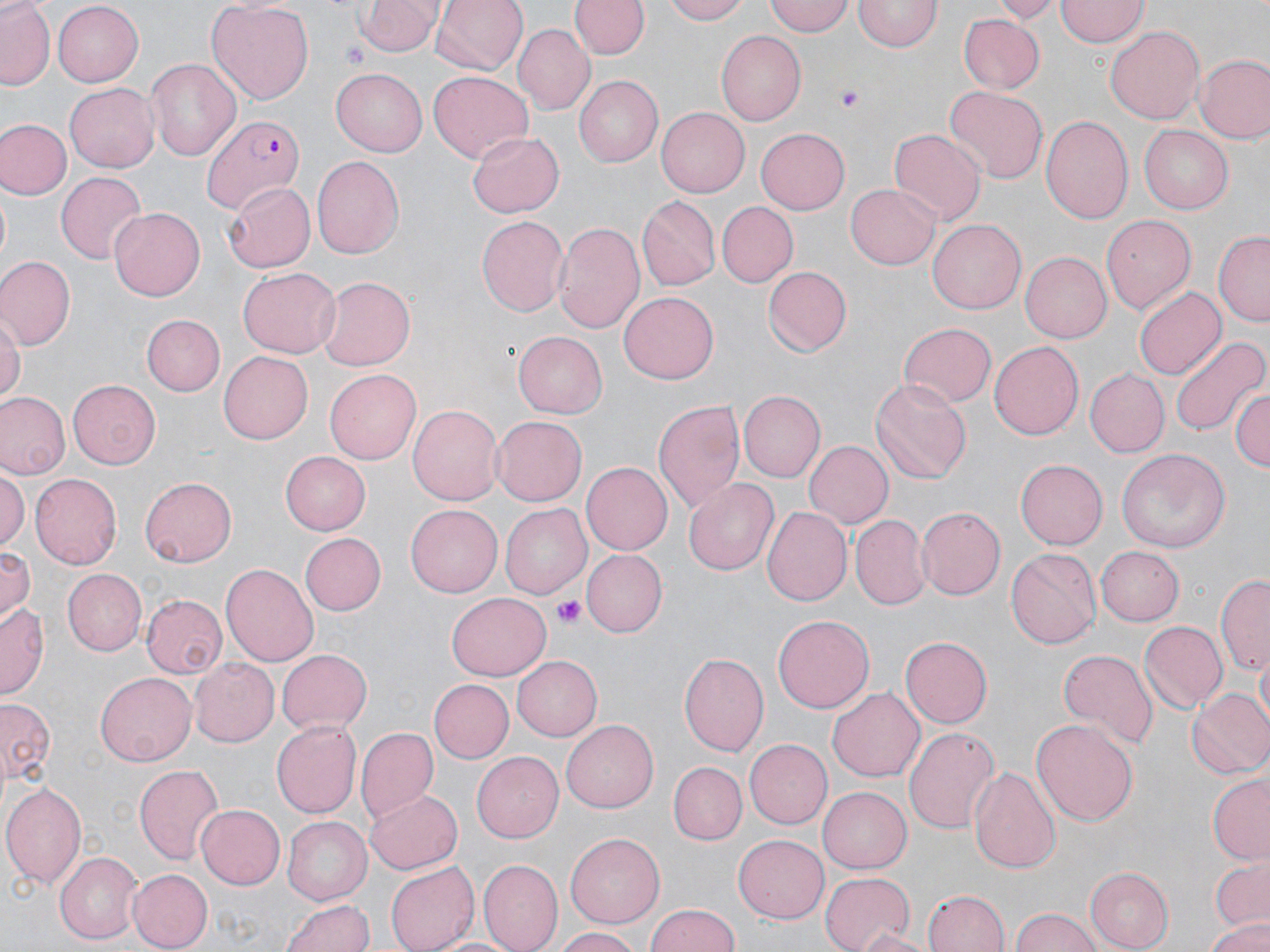
Summary:
  - Coordinate format: approximate bounding boxes as (x1,y1)-(x2,y2) corner pairs in pixels
  - Uninfected red blood cell locations: (1,0)-(53,89), (205,0)-(314,104), (356,0)-(444,56), (430,0)-(528,77), (664,0)-(751,25), (766,0)-(853,36), (991,0)-(1059,22), (1057,0)-(1148,47), (53,1)-(145,86), (571,1)-(647,59), (854,1)-(940,53), (960,13)-(1043,94), (513,25)-(593,114), (1104,27)-(1204,124), (716,32)-(806,124), (1195,53)-(1270,143), (144,57)-(241,161), (331,69)-(428,156), (429,72)-(534,163), (575,75)-(662,167), (65,84)-(160,172), (943,86)-(1047,186), (656,107)-(750,197), (1041,113)-(1134,227), (1,117)-(71,201), (1137,125)-(1231,213), (754,128)-(849,215), (888,128)-(985,225), (468,129)-(564,215), (310,154)-(405,258), (56,172)-(147,265), (223,178)-(317,273), (847,182)-(942,270), (635,198)-(718,291), (716,201)-(797,288), (108,207)-(204,302), (1103,214)-(1195,316), (477,215)-(568,317), (927,219)-(1026,314), (552,221)-(646,337), (1214,232)-(1270,328), (1020,250)-(1111,344), (0,257)-(74,347), (762,266)-(850,356), (238,268)-(340,359), (317,276)-(416,369), (1134,286)-(1226,377), (620,290)-(719,383), (140,313)-(225,395), (0,314)-(22,408), (899,321)-(996,406), (514,331)-(606,418), (1172,337)-(1266,437), (990,341)-(1084,439), (217,352)-(311,443), (326,369)-(421,465), (1086,369)-(1169,456), (870,377)-(971,484), (68,380)-(162,468), (1230,383)-(1269,474), (741,391)-(825,482), (1,392)-(69,480), (652,397)-(746,514), (408,402)-(501,508), (492,417)-(586,504), (804,439)-(893,529), (1116,446)-(1230,553), (279,451)-(369,535), (1015,460)-(1106,549), (582,462)-(671,554), (0,469)-(27,553), (29,473)-(120,569), (141,477)-(237,566), (684,478)-(779,577), (499,503)-(592,599), (405,505)-(501,598), (763,505)-(850,606), (915,506)-(1005,600), (853,515)-(928,609), (298,533)-(384,615), (1,544)-(34,622), (1097,545)-(1184,626), (1008,549)-(1100,650), (582,550)-(666,638), (222,562)-(318,667), (61,567)-(146,655), (1216,573)-(1270,675), (446,593)-(551,681), (140,594)-(226,678), (0,600)-(49,696), (771,614)-(874,716), (1137,621)-(1226,714), (899,636)-(991,728), (277,648)-(371,736), (1056,648)-(1156,752), (677,650)-(770,760), (1254,653)-(1270,726), (513,655)-(603,740), (189,658)-(278,748), (95,670)-(197,766), (430,677)-(512,763), (829,689)-(925,781), (1186,689)-(1270,779), (1,696)-(54,790), (1032,716)-(1138,829), (561,718)-(659,813), (272,720)-(364,819), (356,726)-(438,821), (903,726)-(1001,834), (744,740)-(830,829), (472,751)-(563,842), (133,761)-(224,865), (666,761)-(747,845), (967,765)-(1063,876), (1208,773)-(1270,865), (1,782)-(87,890), (818,787)-(911,873), (365,789)-(462,875), (198,802)-(285,890), (281,817)-(370,906), (735,833)-(830,922), (565,834)-(663,928), (55,850)-(143,942), (1210,858)-(1269,932), (479,860)-(562,952), (385,861)-(480,952), (1085,867)-(1172,952), (127,869)-(212,950), (818,871)-(915,952), (924,889)-(1010,951), (281,895)-(373,952), (644,905)-(742,952), (1009,907)-(1103,952), (1206,914)-(1270,951), (550,927)-(645,952), (854,927)-(943,952), (425,935)-(523,952)
  - Plasmodium falciparum-infected red blood cell locations: (200,112)-(309,210)
  - Platelet locations: (338,44)-(374,70), (837,87)-(864,108), (552,595)-(584,627)
  - Slide-level diagnosis: Plasmodium falciparum
  - Magnification: 1000x
  - Field of view: single
  - Preparation: thin blood smear
  - Image size: 1270×952 pixels
  - Stain: May-Grünwald-Giemsa
  - Modality: light microscopy